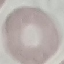
Summary:
  - Result: no malaria parasites detected
  - Stain: Giemsa
  - Preparation: thin smear
  - Capture: smartphone through the microscope eyepiece
  - Image type: automatically extracted cell patch, resized to 64 × 64 pixels